State the blood parasite species.
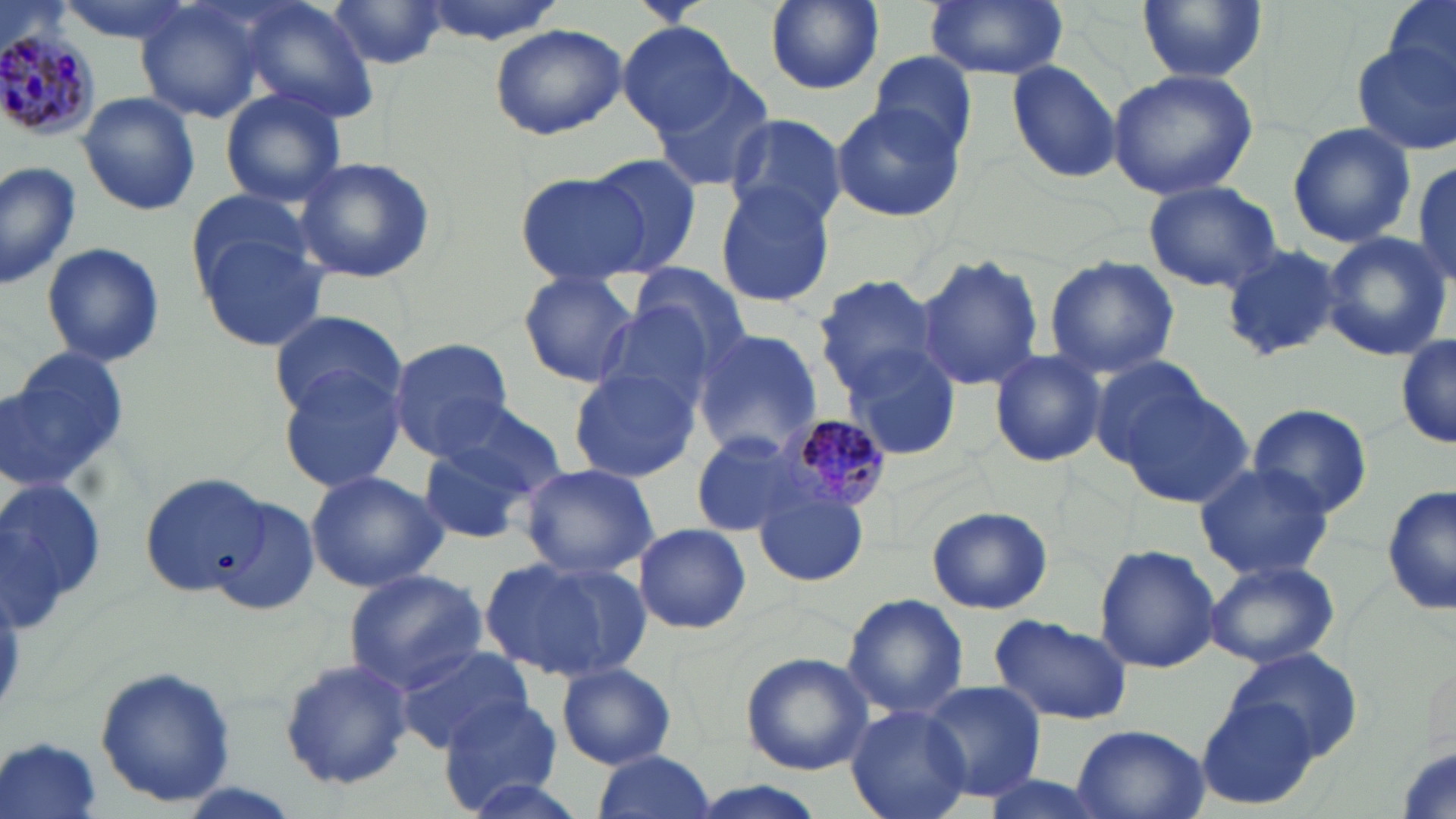
Plasmodium malariae.

Approximate bounding boxes as named x1/y1/x2/y2 corners in pixels. Plasmodium malariae-infected red blood cell locations: (x1=0, y1=25, x2=101, y2=141), (x1=778, y1=412, x2=893, y2=510). Uninfected red blood cell locations: (x1=52, y1=0, x2=201, y2=42), (x1=414, y1=0, x2=568, y2=44), (x1=765, y1=0, x2=883, y2=93), (x1=921, y1=0, x2=1070, y2=81), (x1=1137, y1=0, x2=1265, y2=83), (x1=1378, y1=0, x2=1456, y2=93), (x1=237, y1=1, x2=376, y2=118), (x1=327, y1=1, x2=448, y2=69), (x1=137, y1=4, x2=267, y2=121), (x1=619, y1=21, x2=739, y2=134), (x1=488, y1=25, x2=626, y2=139), (x1=1351, y1=37, x2=1456, y2=158), (x1=867, y1=49, x2=979, y2=160), (x1=1316, y1=54, x2=1430, y2=218), (x1=1006, y1=59, x2=1124, y2=185), (x1=1107, y1=68, x2=1258, y2=201), (x1=646, y1=70, x2=776, y2=193), (x1=220, y1=88, x2=347, y2=208), (x1=76, y1=92, x2=200, y2=215), (x1=831, y1=100, x2=965, y2=225), (x1=724, y1=113, x2=845, y2=228), (x1=1286, y1=122, x2=1418, y2=248), (x1=581, y1=153, x2=703, y2=277), (x1=1409, y1=156, x2=1456, y2=287), (x1=292, y1=157, x2=438, y2=285), (x1=0, y1=159, x2=78, y2=291), (x1=513, y1=172, x2=647, y2=286), (x1=1141, y1=178, x2=1283, y2=292), (x1=713, y1=182, x2=837, y2=307), (x1=184, y1=187, x2=319, y2=293), (x1=1318, y1=232, x2=1452, y2=360), (x1=197, y1=233, x2=330, y2=352), (x1=40, y1=240, x2=166, y2=369), (x1=1219, y1=245, x2=1345, y2=364), (x1=916, y1=253, x2=1046, y2=393), (x1=1043, y1=256, x2=1179, y2=379), (x1=626, y1=261, x2=759, y2=370), (x1=517, y1=270, x2=638, y2=388), (x1=810, y1=274, x2=944, y2=396), (x1=592, y1=302, x2=720, y2=411), (x1=265, y1=308, x2=404, y2=418), (x1=690, y1=329, x2=823, y2=458), (x1=1394, y1=330, x2=1454, y2=452), (x1=388, y1=337, x2=515, y2=457), (x1=1, y1=349, x2=130, y2=496), (x1=987, y1=349, x2=1105, y2=468), (x1=847, y1=352, x2=961, y2=460), (x1=1088, y1=356, x2=1227, y2=478), (x1=275, y1=364, x2=409, y2=492), (x1=567, y1=367, x2=700, y2=483), (x1=1119, y1=380, x2=1254, y2=511), (x1=430, y1=400, x2=568, y2=505), (x1=1245, y1=403, x2=1375, y2=520), (x1=414, y1=431, x2=548, y2=548), (x1=689, y1=431, x2=811, y2=538), (x1=1193, y1=461, x2=1335, y2=581), (x1=516, y1=463, x2=659, y2=578), (x1=304, y1=469, x2=447, y2=593), (x1=138, y1=471, x2=270, y2=598), (x1=139, y1=472, x2=268, y2=595), (x1=754, y1=485, x2=871, y2=587), (x1=1382, y1=485, x2=1455, y2=619), (x1=211, y1=494, x2=323, y2=620), (x1=925, y1=505, x2=1053, y2=615), (x1=633, y1=522, x2=750, y2=635), (x1=1094, y1=542, x2=1219, y2=674), (x1=484, y1=554, x2=647, y2=682), (x1=1204, y1=559, x2=1339, y2=669), (x1=343, y1=568, x2=487, y2=689), (x1=842, y1=593, x2=969, y2=718), (x1=989, y1=616, x2=1132, y2=726), (x1=395, y1=648, x2=532, y2=754), (x1=1230, y1=649, x2=1363, y2=762), (x1=739, y1=652, x2=875, y2=776), (x1=278, y1=657, x2=414, y2=791), (x1=555, y1=661, x2=678, y2=770), (x1=95, y1=664, x2=238, y2=808), (x1=916, y1=680, x2=1049, y2=805), (x1=1194, y1=692, x2=1318, y2=808), (x1=441, y1=695, x2=564, y2=812), (x1=843, y1=705, x2=973, y2=819), (x1=1068, y1=723, x2=1210, y2=819), (x1=0, y1=736, x2=105, y2=819), (x1=589, y1=748, x2=717, y2=819), (x1=971, y1=772, x2=1116, y2=819), (x1=454, y1=776, x2=593, y2=819), (x1=689, y1=781, x2=824, y2=819). Captured at 1000x magnification. Single field of view. Thin blood film. Image is 1456×819 pixels. May-Grünwald-Giemsa-stained preparation. Light microscopy.